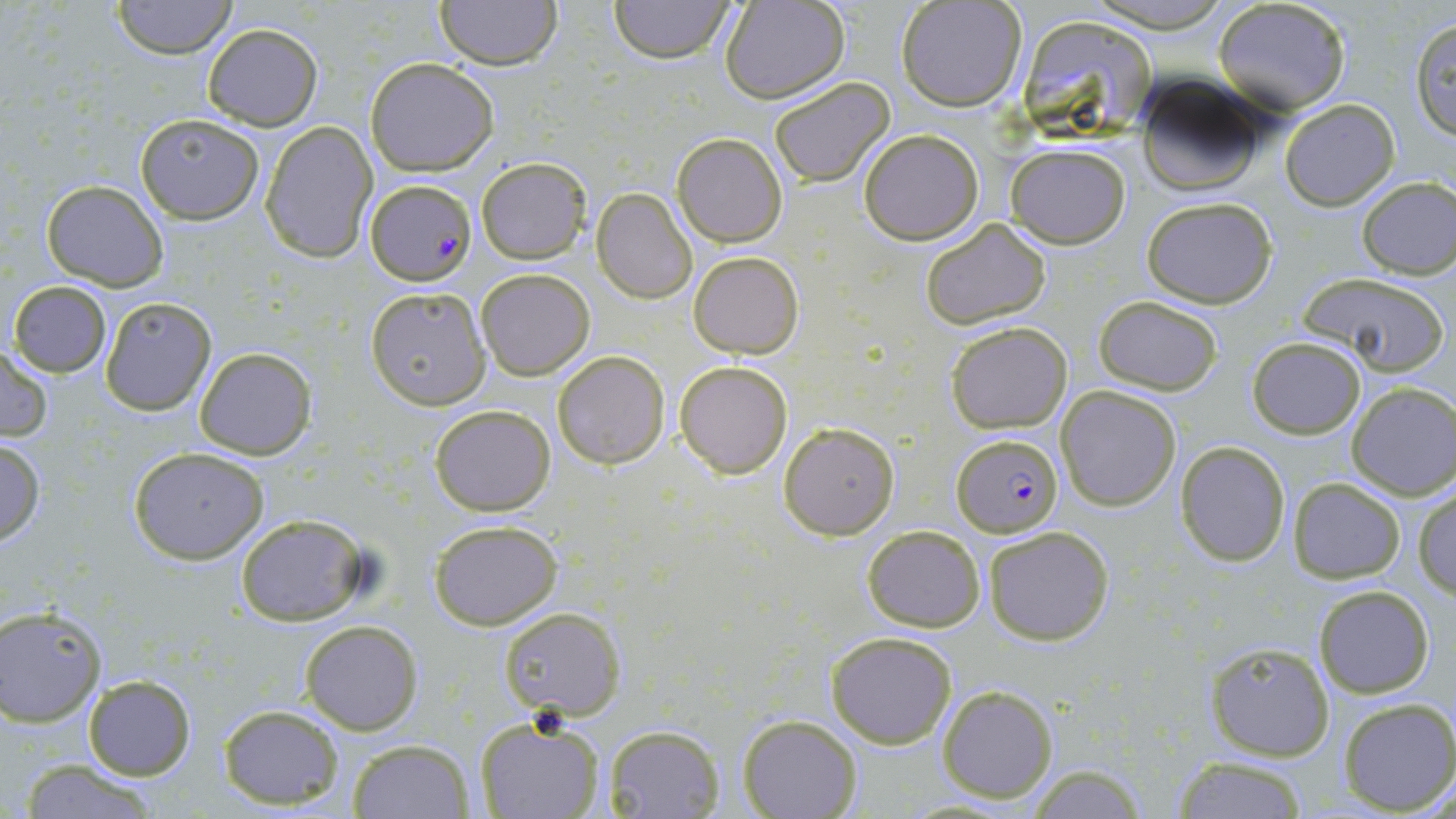

Summary:
  - Coordinate format: approximate bounding boxes as (x1, y1, x2, y2) in pixels
  - Plasmodium falciparum-infected red blood cell locations: (366, 182, 472, 284), (953, 434, 1061, 537)
  - Uninfected red blood cell locations: (112, 0, 238, 59), (434, 0, 562, 70), (608, 0, 737, 64), (1082, 0, 1236, 31), (720, 1, 849, 103), (897, 1, 1027, 111), (1213, 1, 1352, 115), (1015, 14, 1158, 143), (1408, 15, 1456, 139), (202, 23, 323, 130), (364, 57, 499, 176), (1133, 74, 1268, 196), (768, 76, 895, 187), (1279, 99, 1399, 209), (136, 114, 264, 223), (261, 121, 378, 263), (857, 129, 984, 244), (673, 133, 787, 247), (1006, 142, 1131, 247), (477, 157, 592, 263), (1356, 176, 1456, 279), (41, 178, 168, 290), (592, 187, 698, 303), (1139, 196, 1278, 308), (917, 219, 1053, 331), (689, 251, 803, 358), (476, 269, 595, 381), (1297, 272, 1449, 377), (8, 281, 111, 377), (365, 286, 490, 409), (1092, 295, 1224, 395), (100, 299, 215, 416), (944, 320, 1073, 433), (1247, 336, 1365, 439), (0, 344, 53, 442), (194, 348, 316, 460), (552, 351, 670, 469), (674, 359, 794, 479), (1346, 383, 1456, 499), (1056, 385, 1181, 512), (429, 403, 556, 515), (780, 423, 898, 538), (0, 438, 45, 547), (1175, 441, 1291, 568), (129, 448, 270, 565), (1287, 478, 1407, 585), (1414, 486, 1455, 600), (233, 514, 372, 624), (428, 519, 563, 630), (862, 524, 984, 631), (982, 527, 1114, 645), (1312, 584, 1434, 697), (1, 606, 106, 725), (500, 607, 626, 719), (299, 621, 422, 735), (826, 631, 957, 749), (1202, 640, 1336, 761), (81, 676, 195, 780), (937, 684, 1058, 803), (1337, 698, 1456, 814), (217, 703, 344, 809), (737, 714, 861, 819), (474, 716, 607, 819), (603, 724, 724, 818), (347, 739, 475, 818), (1170, 755, 1310, 819), (20, 758, 161, 819), (1021, 766, 1150, 818)
  - Slide-level diagnosis: Plasmodium falciparum
  - Magnification: 1000x
  - Image size: 1456×819 pixels
  - Stain: May-Grünwald-Giemsa
  - Preparation: thin blood film
  - Modality: light microscopy
  - Field of view: one of a larger specimen